State the blood parasite species.
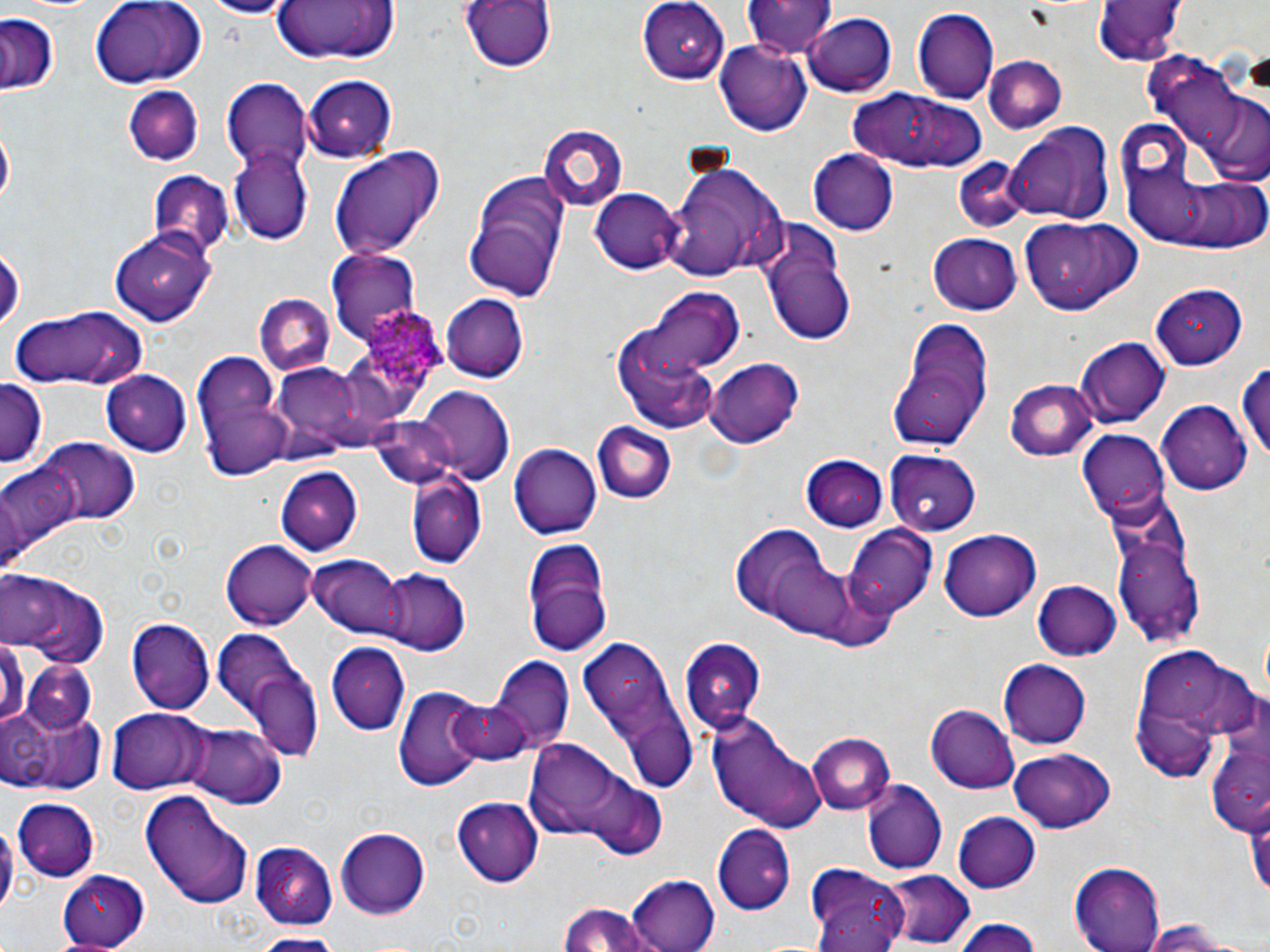

Plasmodium ovale.

stain = May-Grünwald-Giemsa
modality = light microscopy
Plasmodium ovale-infected red blood cell locations = approximate bounding boxes as (x1, y1, x2, y2) in pixels: (362, 302, 448, 395)
field of view = one of a larger specimen
preparation = thin blood film
image size = 1270×952 pixels
uninfected red blood cell locations = approximate bounding boxes as (x1, y1, x2, y2) in pixels: (193, 0, 298, 17), (266, 0, 403, 65), (457, 0, 559, 74), (636, 0, 728, 83), (741, 0, 837, 59), (5, 1, 107, 16), (87, 1, 208, 86), (1093, 2, 1182, 67), (911, 9, 998, 103), (803, 12, 897, 97), (0, 14, 62, 96), (716, 40, 814, 134), (1145, 50, 1268, 184), (984, 56, 1067, 133), (302, 73, 398, 160), (222, 79, 313, 174), (124, 83, 204, 164), (851, 91, 990, 174), (1003, 121, 1115, 227), (1, 124, 14, 214), (539, 126, 626, 211), (326, 143, 446, 259), (808, 149, 900, 236), (231, 151, 312, 243), (666, 156, 786, 283), (952, 159, 1031, 235), (146, 169, 234, 258), (463, 171, 569, 302), (591, 188, 685, 272), (757, 217, 857, 343), (1019, 217, 1141, 316), (109, 226, 217, 325), (928, 234, 1023, 316), (0, 242, 24, 337), (327, 249, 421, 348), (1153, 284, 1249, 370), (643, 290, 744, 379), (252, 293, 334, 377), (440, 293, 527, 382), (613, 295, 737, 428), (11, 306, 147, 392), (892, 318, 997, 451), (1076, 337, 1171, 429), (192, 357, 291, 480), (705, 358, 803, 446), (264, 359, 384, 463), (1236, 361, 1270, 469), (103, 370, 193, 455), (1007, 379, 1098, 463), (0, 381, 46, 471), (418, 388, 513, 483), (1158, 401, 1252, 492), (366, 416, 458, 493), (592, 422, 677, 504), (1076, 431, 1168, 517), (37, 439, 138, 527), (508, 445, 602, 539), (883, 451, 979, 534), (801, 457, 891, 532), (1, 463, 78, 567), (275, 466, 363, 556), (404, 471, 487, 568), (1108, 518, 1207, 648), (844, 523, 938, 616), (723, 524, 862, 637), (938, 528, 1042, 621), (521, 537, 612, 655), (224, 540, 316, 629), (308, 554, 407, 640), (376, 568, 470, 655), (3, 575, 111, 667), (1031, 580, 1123, 661), (126, 618, 214, 713), (210, 629, 322, 761), (576, 637, 694, 792), (676, 639, 766, 736), (0, 642, 30, 724), (328, 642, 410, 735), (1133, 647, 1261, 776), (490, 657, 574, 752), (21, 660, 97, 736), (997, 660, 1091, 748), (395, 686, 490, 790), (445, 696, 531, 766), (5, 701, 106, 792), (926, 705, 1021, 794), (108, 708, 210, 795), (706, 713, 829, 833), (180, 725, 287, 809), (806, 733, 895, 817), (519, 740, 660, 858), (1009, 748, 1117, 833), (579, 777, 669, 860), (863, 781, 947, 874), (143, 788, 254, 911), (452, 797, 544, 887), (12, 800, 101, 878), (952, 812, 1041, 893), (712, 825, 797, 915), (334, 827, 432, 919), (249, 842, 337, 927), (1069, 862, 1166, 952), (56, 868, 152, 947), (807, 868, 912, 952), (883, 869, 976, 946), (626, 873, 722, 951), (558, 901, 660, 952), (949, 916, 1049, 951), (1135, 920, 1258, 952), (249, 933, 348, 952)
magnification = 1000x